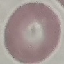
Malaria status: uninfected. Automatically extracted cell patch, resized to 64 × 64 pixels. Thin smear of blood. Acquired by smartphone through the microscope eyepiece. Giemsa stain.